Assess the morphology of the red blood cells.
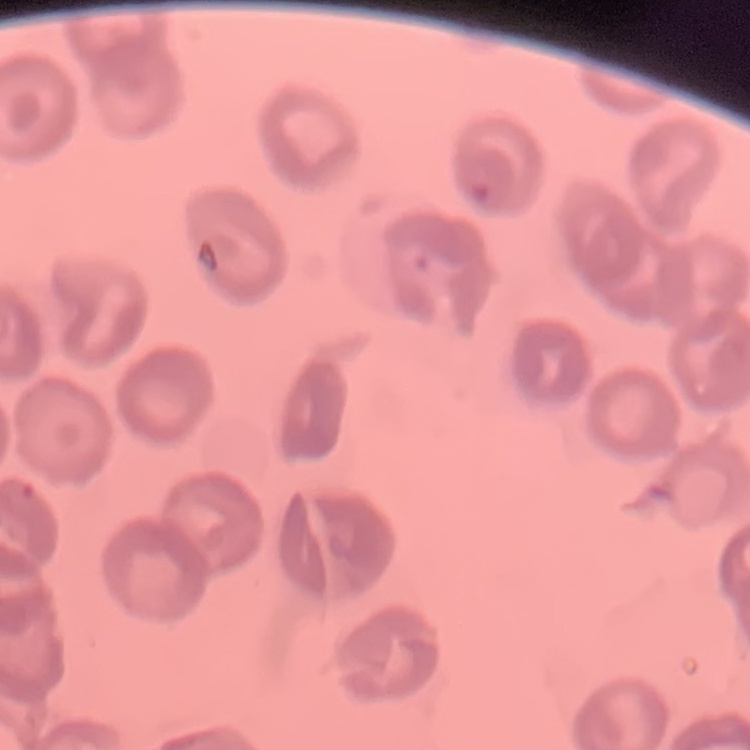
They show no rouleaux formation.

stain = Field's or Giemsa
preparation = thin peripheral smear
image type = square crop of a larger photomicrograph